Assess this cell for malaria.
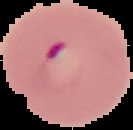
Parasitized.

Image is 133×130 pixels. Segmented cell region on a black background. From a thin blood smear.